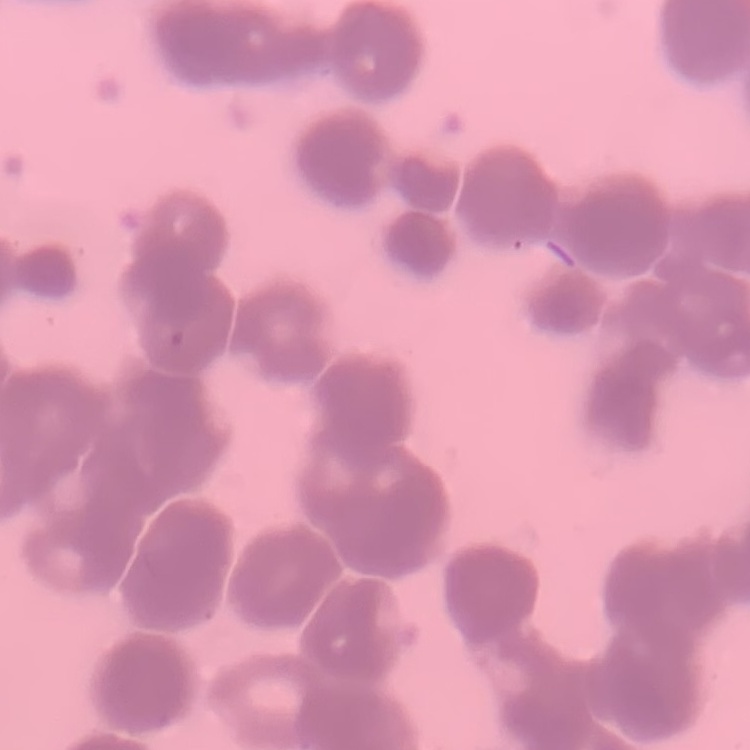
Summary:
  - Red blood cell morphology: rouleaux formation
  - Preparation: thin peripheral smear
  - Stain: Field's or Giemsa
  - Image type: square crop of a larger photomicrograph